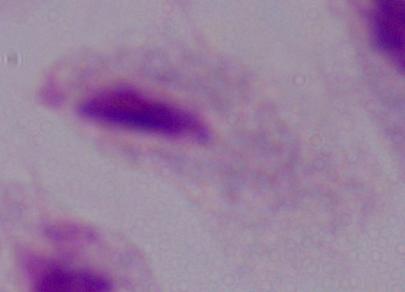

Photomicrograph. A trichomonad is seen. 1000x magnification.